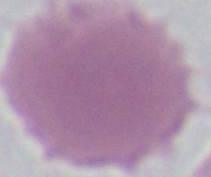

Photomicrograph. An erythrocyte is seen. Captured at 1000x magnification.